Report the malaria status of this cell.
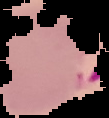

Parasitized.

Image is 109×118 pixels. Segmented cell region on a black background. From a thin blood film.